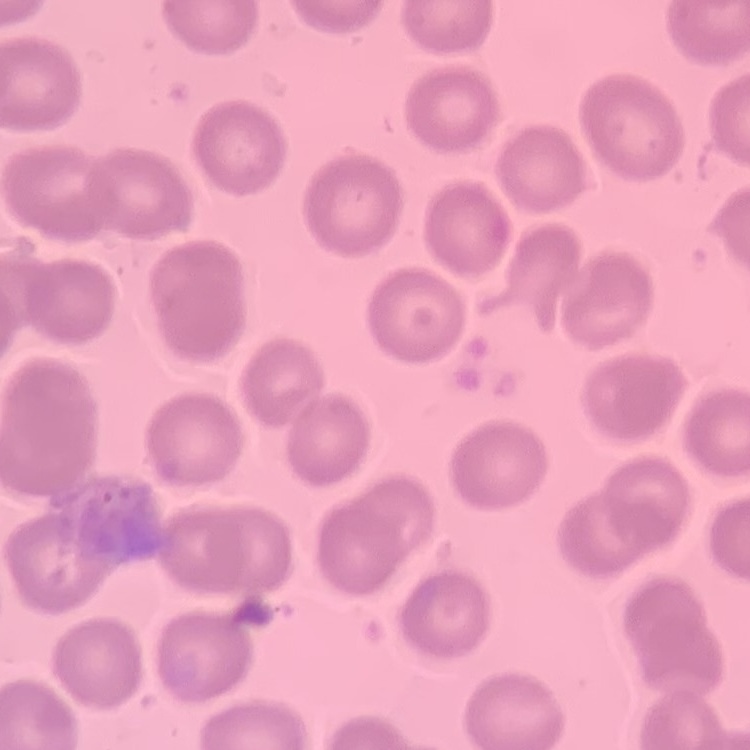
red_blood_cell_morphology: no rouleaux formation
preparation: thin blood smear
image_type: square crop of a larger photomicrograph
stain: Field's or Giemsa